State which cell type is depicted.
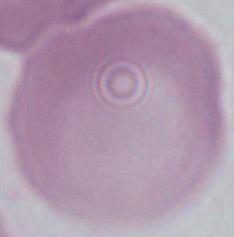
An erythrocyte.

modality: photomicrograph
magnification: 1000x